Locate and identify every blood parasite.
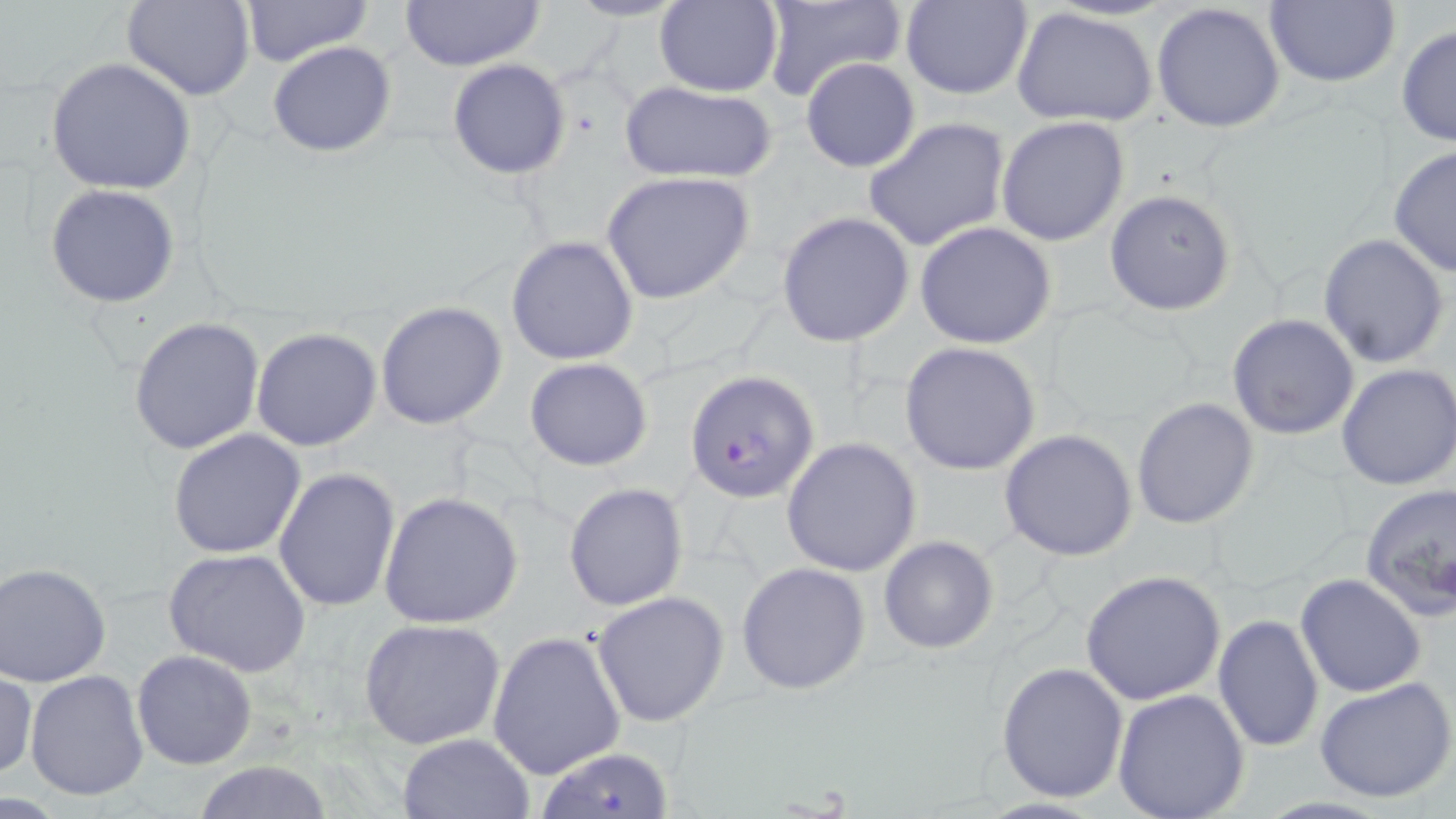
Approximate bounding boxes as (x1,y1)-(x2,y2) corner pairs in pixels.
Plasmodium falciparum-infected red blood cells: (685,368)-(816,503), (537,748)-(675,818).
No Plasmodium ovale, Plasmodium malariae, Plasmodium vivax, Babesia divergens, or Trypanosoma brucei observed.

Summary:
  - Uninfected red blood cell locations: (123,0)-(255,101), (240,0)-(372,65), (397,0)-(548,71), (564,0)-(689,23), (760,0)-(907,106), (654,1)-(782,97), (901,1)-(1033,99), (1263,1)-(1401,88), (1151,2)-(1287,134), (1011,7)-(1158,128), (1396,24)-(1456,149), (267,41)-(398,157), (45,57)-(197,195), (801,58)-(921,173), (447,59)-(571,179), (618,79)-(779,185), (995,115)-(1131,249), (862,116)-(1011,252), (1387,147)-(1456,278), (601,171)-(755,306), (46,184)-(181,307), (1103,187)-(1237,317), (774,211)-(916,346), (915,221)-(1057,349), (1318,233)-(1450,367), (506,234)-(640,365), (375,300)-(508,431), (1227,313)-(1359,439), (128,316)-(265,454), (251,327)-(381,450), (899,341)-(1042,475), (524,356)-(654,471), (1336,362)-(1456,491), (1132,396)-(1260,529), (998,428)-(1138,561), (168,429)-(306,559), (781,437)-(921,577), (273,468)-(401,615), (563,482)-(689,609), (1358,482)-(1456,618), (378,491)-(523,629), (878,536)-(998,655), (163,548)-(312,677), (735,561)-(871,694), (1,563)-(111,686), (1080,569)-(1227,705), (1295,573)-(1427,697), (591,590)-(731,727), (1212,614)-(1324,755), (359,618)-(506,749), (487,631)-(626,780), (130,649)-(258,770), (996,660)-(1130,803), (0,669)-(37,782), (24,670)-(150,802), (1315,676)-(1456,804), (1112,688)-(1250,818), (396,733)-(533,818), (189,759)-(339,817)
  - Slide-level diagnosis: Plasmodium falciparum
  - Image size: 1456×819 pixels
  - Modality: light microscopy
  - Field of view: single
  - Stain: May-Grünwald-Giemsa
  - Preparation: thin blood smear
  - Magnification: 1000x